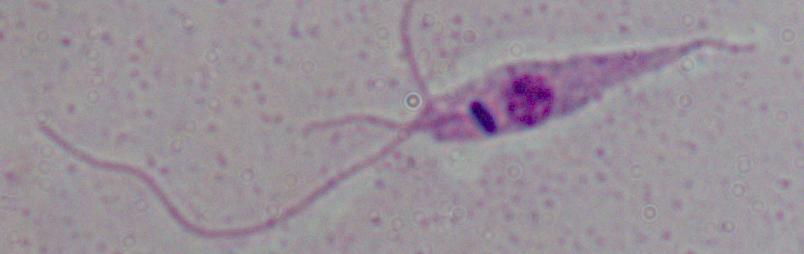 Photomicrograph. 1000x magnification. A Leishmania parasite is seen.